Point out each Plasmodium parasite.
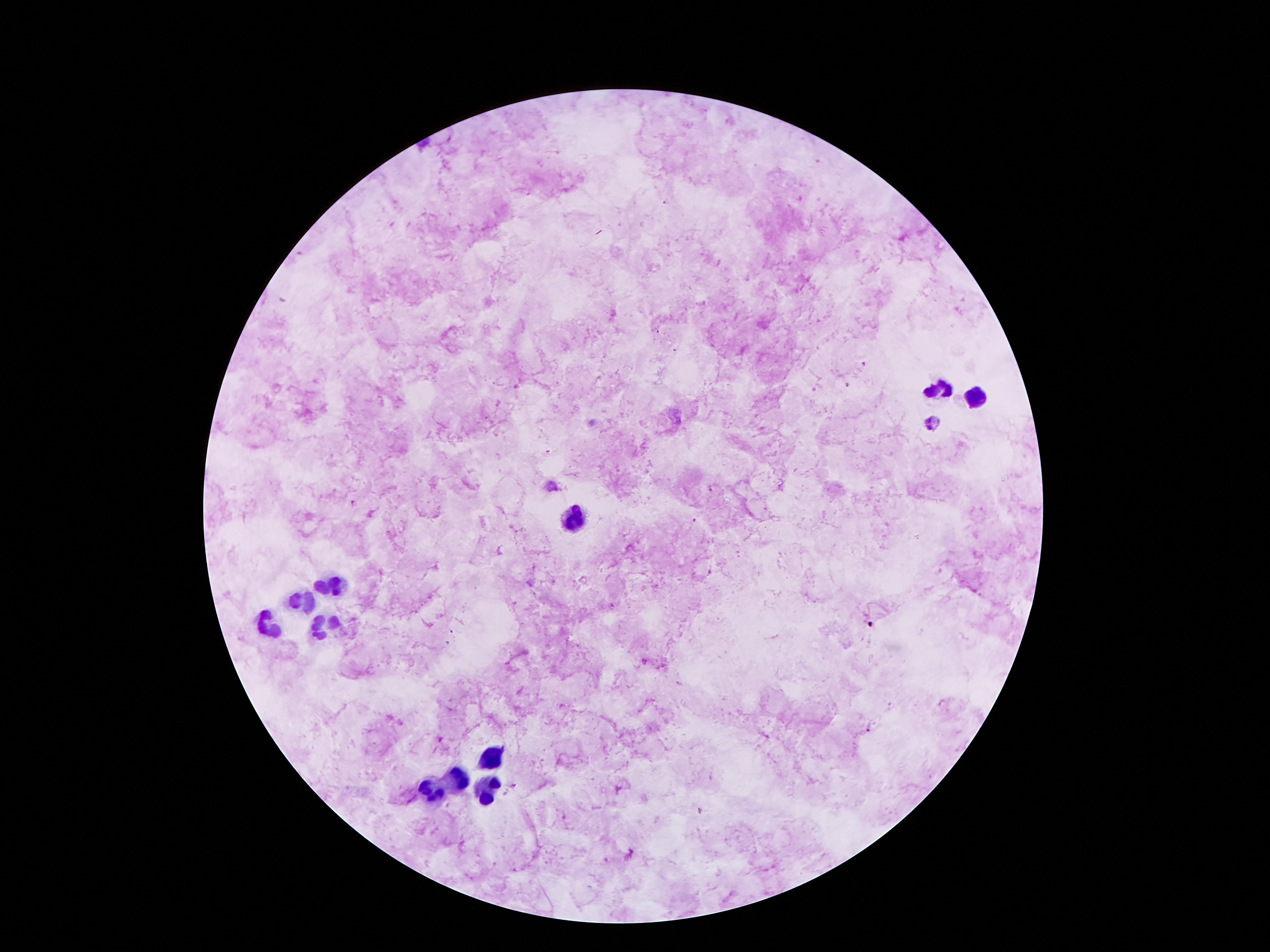
Approximate object centers, in pixels from the top-left corner.
Plasmodium parasites: (x=667, y=201), (x=847, y=386), (x=711, y=491), (x=354, y=505), (x=700, y=811).

Leukocyte locations: (x=941, y=392), (x=976, y=397), (x=575, y=515), (x=333, y=589), (x=304, y=598), (x=325, y=622), (x=265, y=625), (x=490, y=760), (x=460, y=780), (x=428, y=789), (x=488, y=791). Smartphone photograph taken through the microscope eyepiece. 100x magnification. Thick blood smear. Giemsa stain. Image is 1270×952 pixels. One field from this slide. Patient malaria status: positive for Plasmodium falciparum.